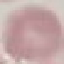
Summary:
  - Result: negative for malaria parasites
  - Capture: smartphone through the microscope eyepiece
  - Image type: cell patch, automatically extracted from a larger field of view and resized to 64 × 64 pixels
  - Stain: Giemsa
  - Preparation: thin blood smear